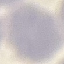
Result: no malaria parasites detected. Thin blood film. Acquired by smartphone through the microscope eyepiece. Giemsa-stained preparation. Automatically extracted cell patch, resized to 64 × 64 pixels.